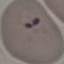

malaria status = parasitized
preparation = thin smear
capture = smartphone camera at the microscope eyepiece
stain = Giemsa
image type = cell patch, automatically extracted from a larger field of view and resized to 64 × 64 pixels